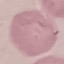 Malaria status: uninfected. Thin blood film. Giemsa stain. Cell patch, automatically extracted from a larger field of view and resized to 64 × 64 pixels. Photographed with a smartphone camera at the microscope eyepiece.